Assess the morphology of the erythrocytes.
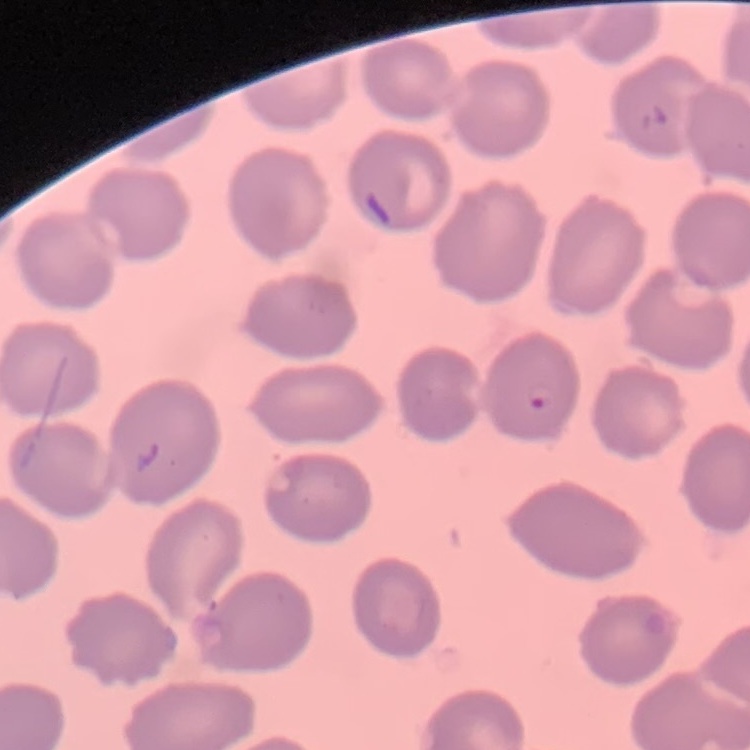

No rouleaux formation.

stain: Field's or Giemsa
preparation: thin blood smear
image_type: square crop of a larger photomicrograph